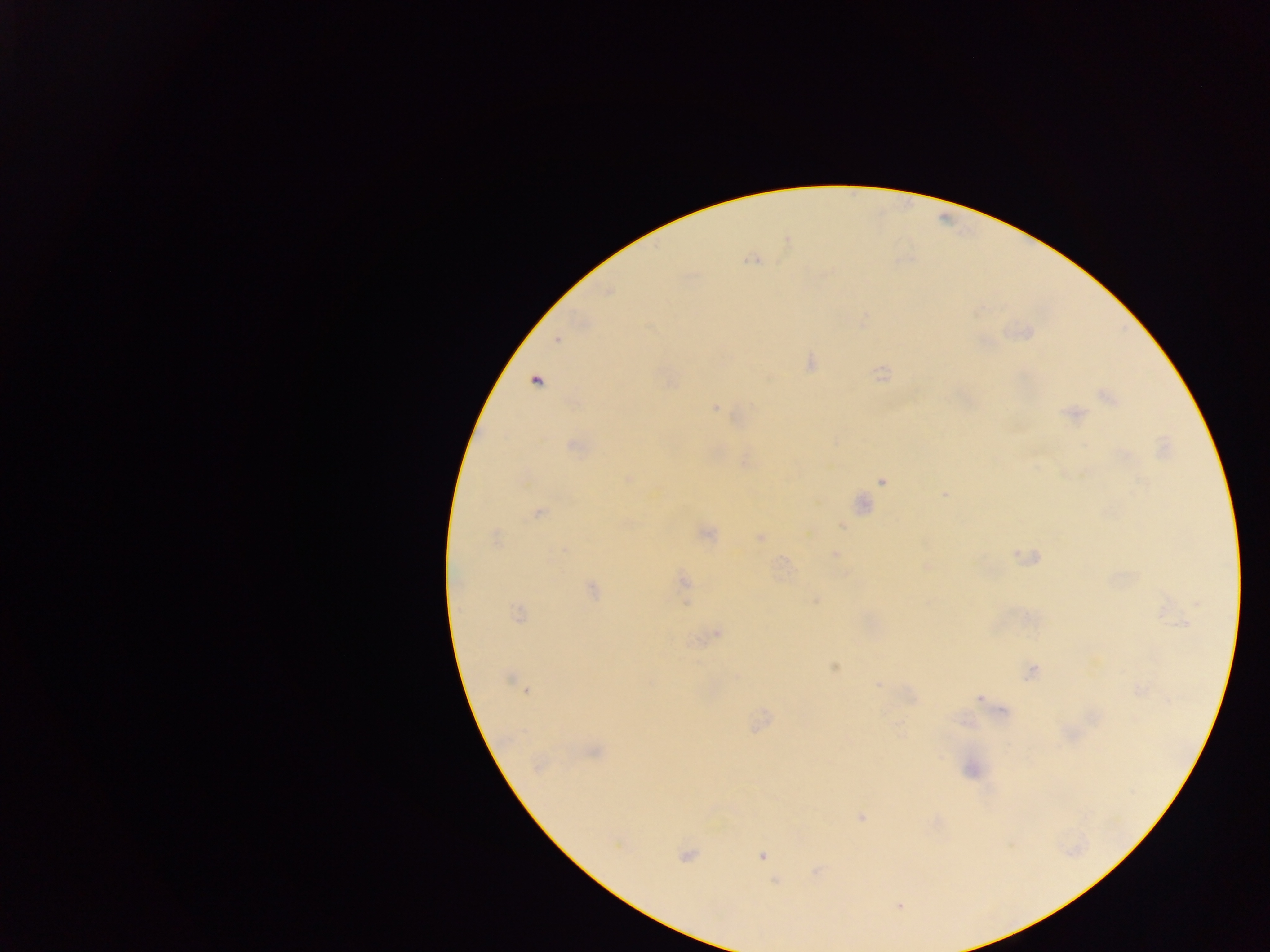
Approximate centers as (x, y) in pixels.
Summary:
  - Malaria parasite locations: (752, 260), (556, 340), (811, 363), (535, 380), (1105, 395), (716, 407), (1073, 415), (574, 446), (628, 478), (882, 481), (945, 494), (862, 504), (538, 513), (842, 526), (706, 533), (494, 536), (760, 538), (565, 549), (835, 555), (684, 581), (592, 590), (815, 601), (1197, 604), (518, 614), (718, 634), (835, 668), (1031, 672), (509, 680), (877, 684), (1141, 690), (526, 691), (978, 699), (594, 752), (539, 765), (860, 818), (685, 857), (762, 857), (775, 881), (899, 905)
  - Country: Ghana
  - Image size: 1270×952 pixels
  - Field of view: single
  - Preparation: thick blood film
  - Capture: mobile-phone photograph through a microscope